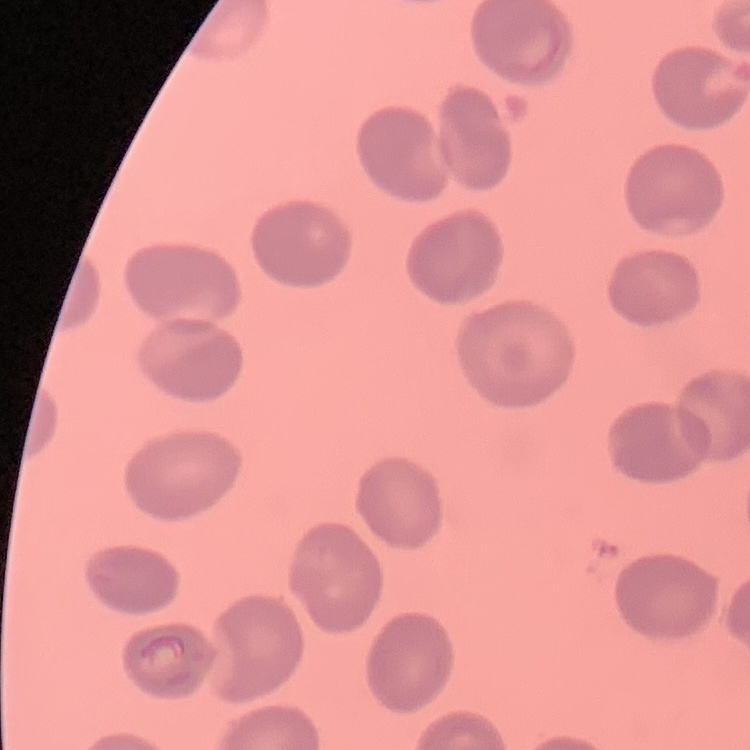

{
  "red_blood_cell_morphology": "no rouleaux formation",
  "stain": "Field's or Giemsa",
  "preparation": "thin peripheral smear",
  "image_type": "one tile cut from a larger photomicrograph"
}